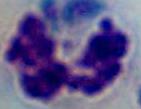
magnification: 1000x
identification: white blood cell
modality: photomicrograph